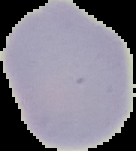

Segmented cell region on a black background. From a thin blood film. Result: no malaria parasites detected. Image is 136×151 pixels.